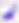

Summary:
  - Identification: Toxoplasma gondii
  - Modality: photomicrograph
  - Magnification: 400x